Identify the cell.
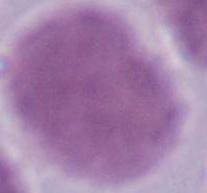
This is an erythrocyte.

Micrograph. Captured at 1000x magnification.